Assess this cell for malaria.
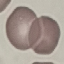
It is uninfected.

image type = automatically extracted cell patch, resized to 64 × 64 pixels
stain = Giemsa
preparation = thin smear
capture = smartphone camera at the microscope eyepiece